Outline each Plasmodium falciparum-infected red blood cell.
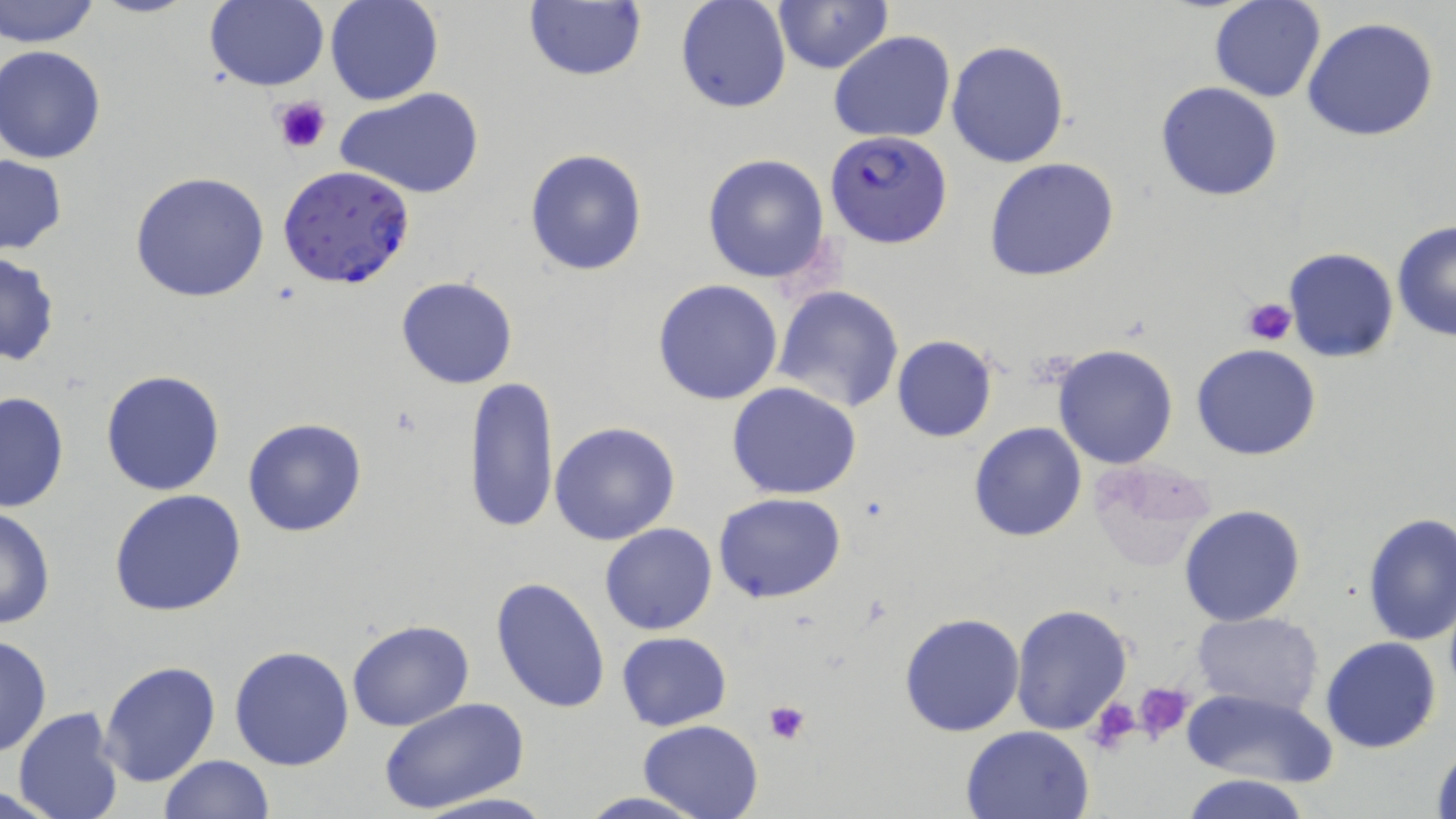
Approximate bounding boxes as (x1, y1, x2, y2) in pixels.
Plasmodium falciparum-infected red blood cells: (826, 131, 950, 248), (279, 162, 415, 290).

Platelet locations: (270, 94, 332, 154), (1241, 297, 1297, 345), (1132, 681, 1193, 742), (1087, 697, 1142, 755), (763, 700, 811, 744). Uninfected red blood cell locations: (1, 0, 101, 48), (325, 0, 444, 106), (676, 0, 791, 114), (771, 0, 893, 73), (204, 1, 328, 91), (522, 1, 647, 84), (1208, 1, 1326, 103), (1302, 16, 1438, 142), (829, 31, 957, 145), (947, 41, 1070, 167), (1, 46, 110, 163), (1156, 82, 1284, 201), (339, 89, 483, 199), (524, 147, 648, 278), (702, 153, 833, 284), (0, 154, 69, 256), (984, 159, 1121, 282), (129, 171, 270, 304), (1393, 219, 1456, 342), (1284, 248, 1399, 362), (0, 252, 61, 366), (396, 276, 517, 389), (652, 280, 783, 405), (773, 285, 904, 413), (892, 334, 997, 441), (1053, 344, 1178, 468), (1192, 344, 1322, 461), (101, 369, 227, 497), (466, 375, 559, 536), (726, 382, 862, 500), (0, 392, 70, 515), (243, 418, 366, 536), (549, 421, 680, 545), (967, 421, 1087, 543), (1090, 460, 1219, 570), (109, 489, 248, 616), (715, 493, 845, 605), (1179, 503, 1307, 626), (0, 507, 56, 631), (1361, 513, 1456, 645), (600, 523, 717, 635), (490, 577, 611, 715), (1009, 603, 1133, 736), (899, 611, 1025, 737), (1191, 612, 1322, 714), (346, 619, 474, 732), (616, 631, 731, 731), (0, 632, 52, 758), (1319, 638, 1441, 754), (228, 644, 355, 771), (99, 661, 220, 788), (1183, 686, 1336, 786), (378, 697, 531, 814), (13, 707, 125, 819), (636, 719, 766, 818), (960, 724, 1097, 818), (1429, 739, 1455, 819), (158, 755, 273, 819), (1183, 773, 1312, 819), (0, 783, 64, 816), (412, 791, 558, 819), (573, 792, 709, 819). Slide-level diagnosis: Plasmodium falciparum. One field of a larger specimen. 1000x magnification. Thin blood smear. Optical microscopy. Image is 1456×819 pixels. May-Grünwald-Giemsa-stained preparation.